State the blood parasite species.
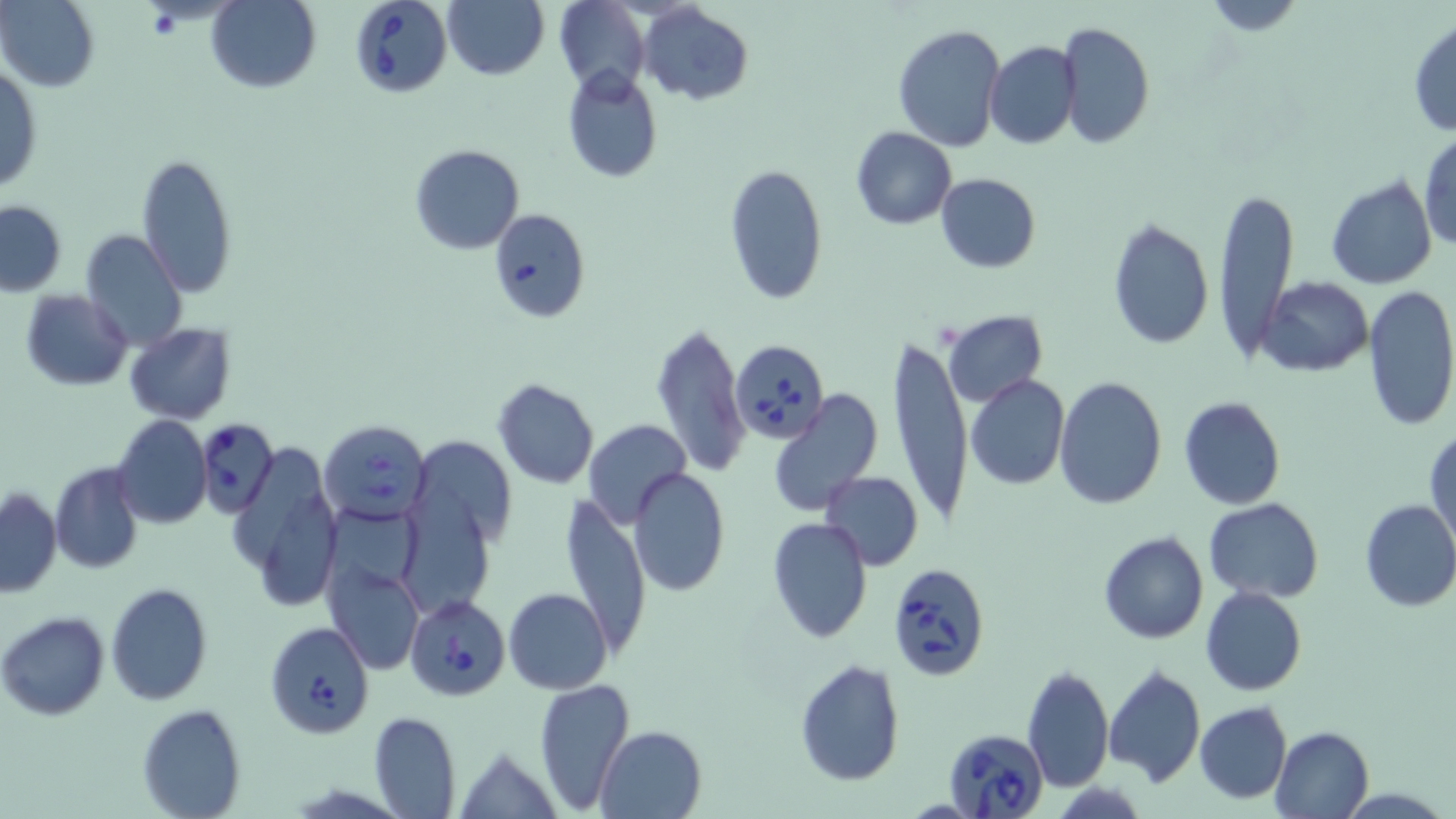

Babesia divergens.

Approximate bounding boxes as (x1,y1)-(x2,y2) corner pairs in pixels. Uninfected red blood cell locations: (1,0)-(99,90), (207,0)-(321,93), (444,0)-(549,80), (553,0)-(648,93), (1193,1)-(1311,34), (639,5)-(753,106), (1408,17)-(1456,139), (1058,21)-(1155,149), (894,23)-(1005,152), (983,41)-(1080,149), (1,67)-(43,193), (561,69)-(663,183), (852,127)-(958,230), (1417,131)-(1455,254), (409,143)-(525,254), (137,153)-(238,299), (725,162)-(826,305), (935,173)-(1041,273), (1325,175)-(1437,290), (1212,188)-(1297,362), (1,200)-(67,296), (488,208)-(589,321), (1105,216)-(1214,351), (80,229)-(187,349), (1259,276)-(1376,376), (1362,285)-(1456,434), (22,290)-(131,390), (941,310)-(1047,408), (125,322)-(235,424), (651,322)-(749,477), (887,333)-(972,530), (965,375)-(1069,489), (1053,376)-(1168,509), (492,378)-(599,488), (767,391)-(884,515), (1177,396)-(1286,510), (111,415)-(211,528), (583,419)-(693,530), (1427,428)-(1456,552), (411,435)-(516,555), (228,442)-(344,616), (48,461)-(144,575), (628,467)-(731,596), (820,471)-(924,570), (1,488)-(62,596), (559,496)-(651,663), (1205,498)-(1324,602), (1358,500)-(1456,613), (767,516)-(874,644), (1098,532)-(1208,644), (325,555)-(424,675), (105,582)-(213,704), (1200,587)-(1307,695), (504,588)-(613,694), (0,611)-(110,721), (793,659)-(905,786), (1021,661)-(1114,791), (1101,663)-(1206,787), (535,677)-(634,813), (1194,701)-(1291,802), (138,703)-(245,818), (368,710)-(460,819), (595,724)-(708,818), (1271,725)-(1375,819), (452,743)-(562,818). Babesia divergens-infected red blood cell locations: (349,0)-(452,98), (728,344)-(826,446), (196,419)-(278,518), (319,419)-(430,526), (886,563)-(993,679), (405,595)-(510,700), (264,620)-(375,739), (944,728)-(1049,819). May-Grünwald-Giemsa stain. Thin blood film. Image is 1456×819 pixels. Optical microscopy. One field of a larger specimen. Captured at 1000x magnification.